Name the parasite shown.
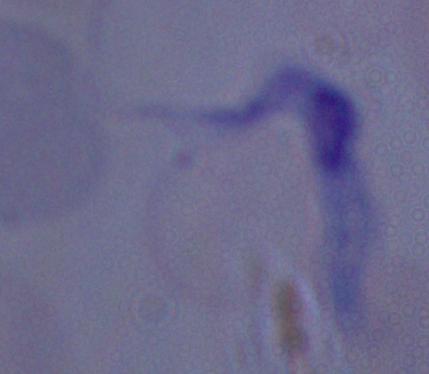
This is a trypanosome.

1000x magnification. Photomicrograph.